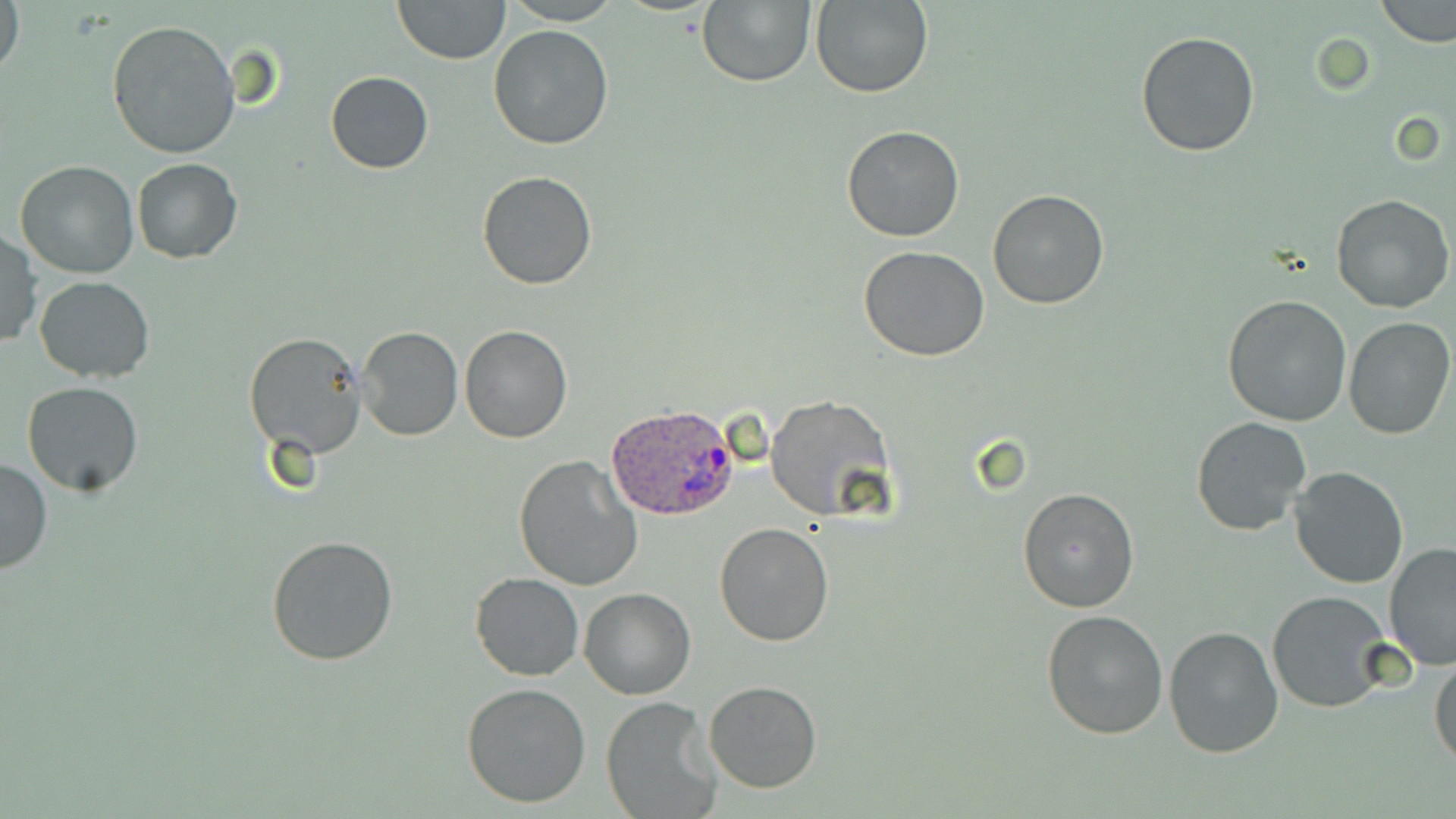
slide-level diagnosis = Plasmodium ovale
preparation = thin blood smear
modality = optical microscopy
stain = May-Grünwald-Giemsa
Plasmodium ovale-infected red blood cell locations = approximate bounding boxes as (x1,y1)-(x2,y2) corner pairs in pixels: (604,402)-(739,523)
field of view = one of a larger specimen
magnification = 1000x
uninfected red blood cell locations = approximate bounding boxes as (x1,y1)-(x2,y2) corner pairs in pixels: (1,0)-(24,82), (392,0)-(511,64), (696,0)-(816,87), (810,0)-(933,98), (1375,0)-(1455,47), (504,1)-(619,25), (107,20)-(240,159), (487,24)-(616,150), (1134,30)-(1260,159), (326,71)-(434,174), (841,124)-(965,242), (131,158)-(242,263), (14,161)-(140,279), (477,171)-(598,291), (988,191)-(1110,309), (1331,194)-(1453,314), (0,231)-(41,349), (859,246)-(990,363), (34,275)-(157,383), (1221,294)-(1352,428), (1342,316)-(1454,439), (458,323)-(573,443), (356,326)-(462,441), (243,332)-(368,460), (22,381)-(143,495), (764,394)-(895,522), (1191,417)-(1311,537), (0,455)-(52,576), (512,455)-(643,593), (1289,464)-(1409,588), (1017,486)-(1142,614), (715,523)-(833,646), (266,534)-(400,668), (1383,541)-(1456,670), (470,573)-(584,681), (579,587)-(695,701), (1267,591)-(1395,714), (1040,608)-(1168,741), (1164,626)-(1285,759), (1429,652)-(1456,768), (703,680)-(823,794), (461,682)-(592,809), (601,697)-(721,818)
image size = 1456×819 pixels